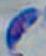

{
  "modality": "photomicrograph",
  "magnification": "1000x",
  "identification": "Toxoplasma gondii"
}